Describe the morphology of the erythrocytes.
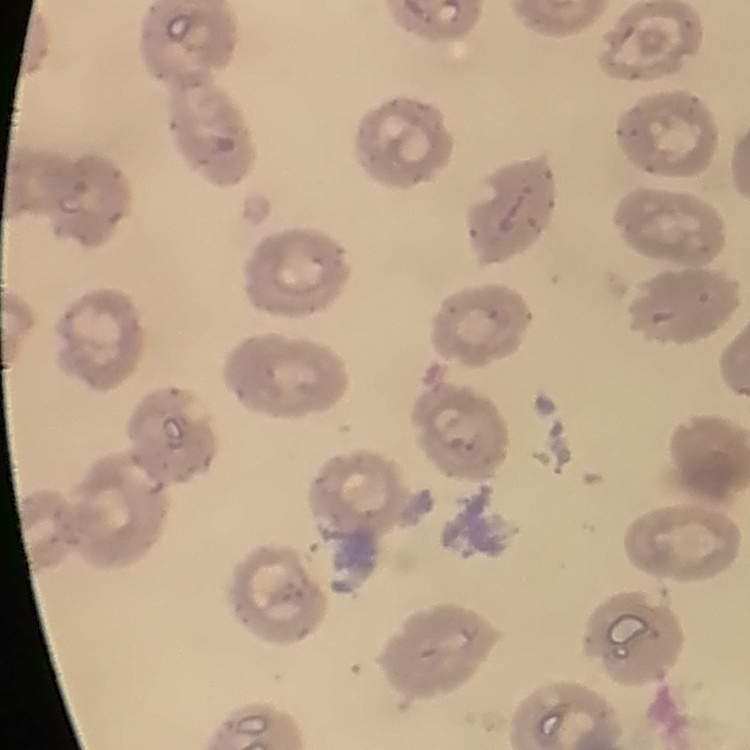
They show no rouleaux formation.

{
  "stain": "Field's or Giemsa",
  "image_type": "square crop of a larger photomicrograph",
  "preparation": "thin blood film"
}